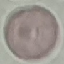

result: no malaria parasites seen
preparation: thin blood smear
image_type: cell patch, automatically extracted from a larger field of view and resized to 64 × 64 pixels
stain: Giemsa
capture: smartphone camera at the microscope eyepiece